Locate every leukocyte (white blood cell).
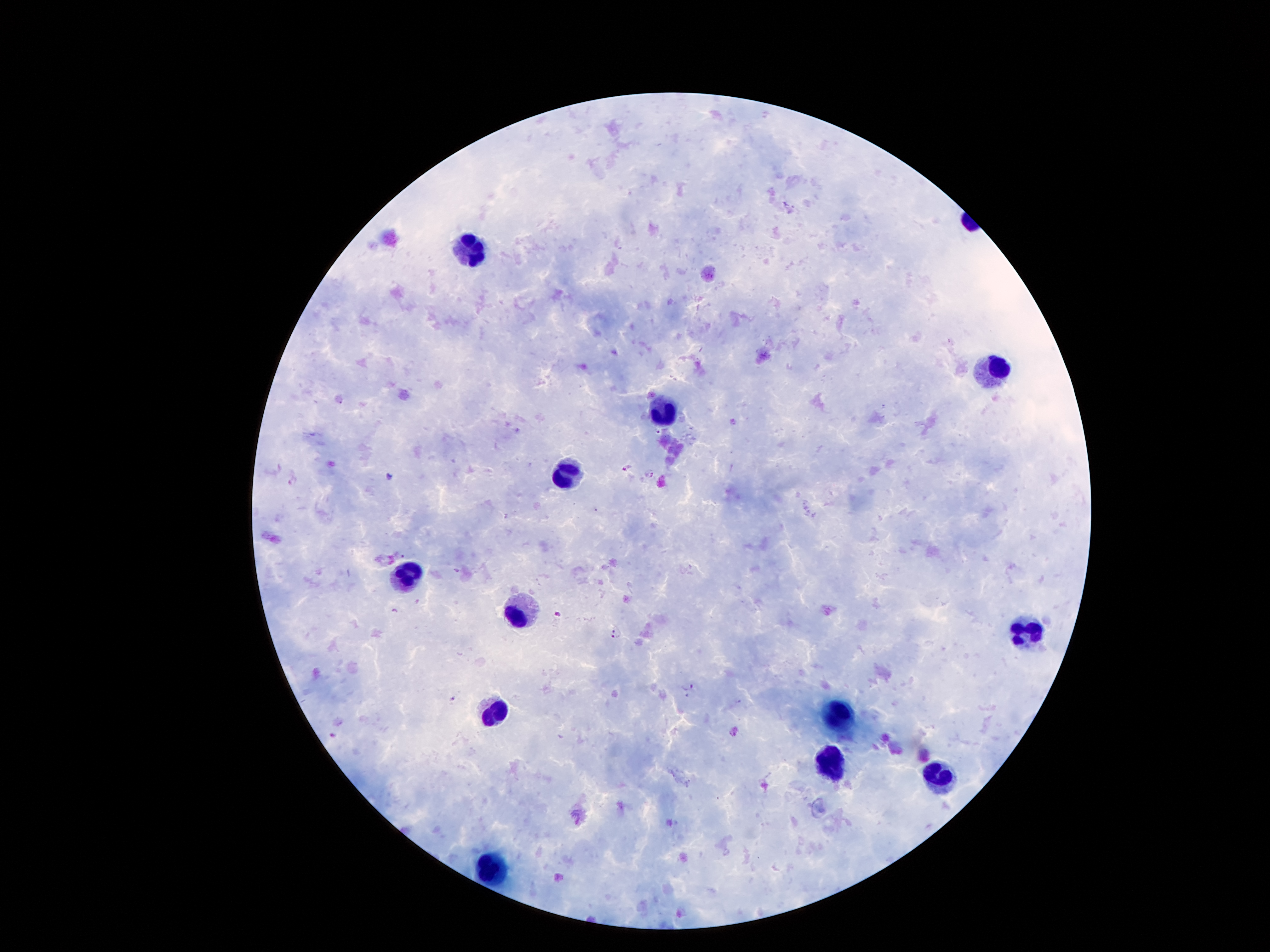

Approximate object centers, in pixels from the top-left corner.
Leukocytes: (x=471, y=249), (x=993, y=366), (x=661, y=408), (x=566, y=474), (x=405, y=571), (x=519, y=615), (x=1028, y=633), (x=495, y=712), (x=840, y=713), (x=831, y=764), (x=937, y=775), (x=489, y=863).

Malaria parasite locations: (x=733, y=421), (x=657, y=433), (x=627, y=467), (x=651, y=474), (x=390, y=477), (x=403, y=556), (x=459, y=570), (x=557, y=614), (x=615, y=630), (x=614, y=638), (x=688, y=688), (x=453, y=699), (x=334, y=735). One field from this slide. Image is 1270×952 pixels. Smartphone photograph taken through the microscope eyepiece. Patient malaria status: infected with Plasmodium falciparum. Giemsa stain. Thick blood smear. 100x magnification.